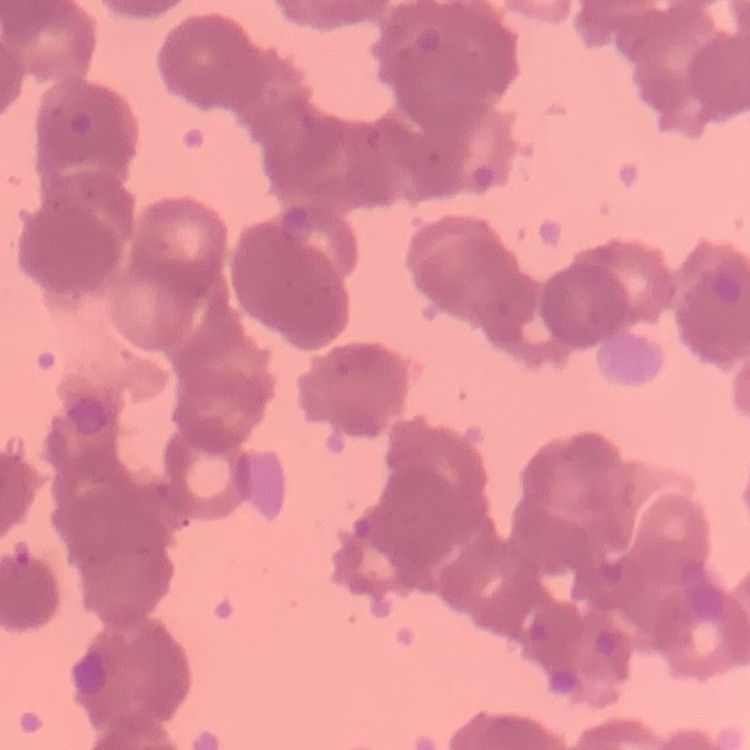 The red blood cells show rouleaux formation. Square crop of a larger photomicrograph. Field's or Giemsa stain. Thin peripheral smear.